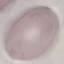

Result: no malaria parasites seen. Photographed with a smartphone camera at the microscope eyepiece. Giemsa-stained preparation. Cell patch, automatically extracted from a larger field of view and resized to 64 × 64 pixels. Thin smear of blood.